Locate every blood parasite and identify its species.
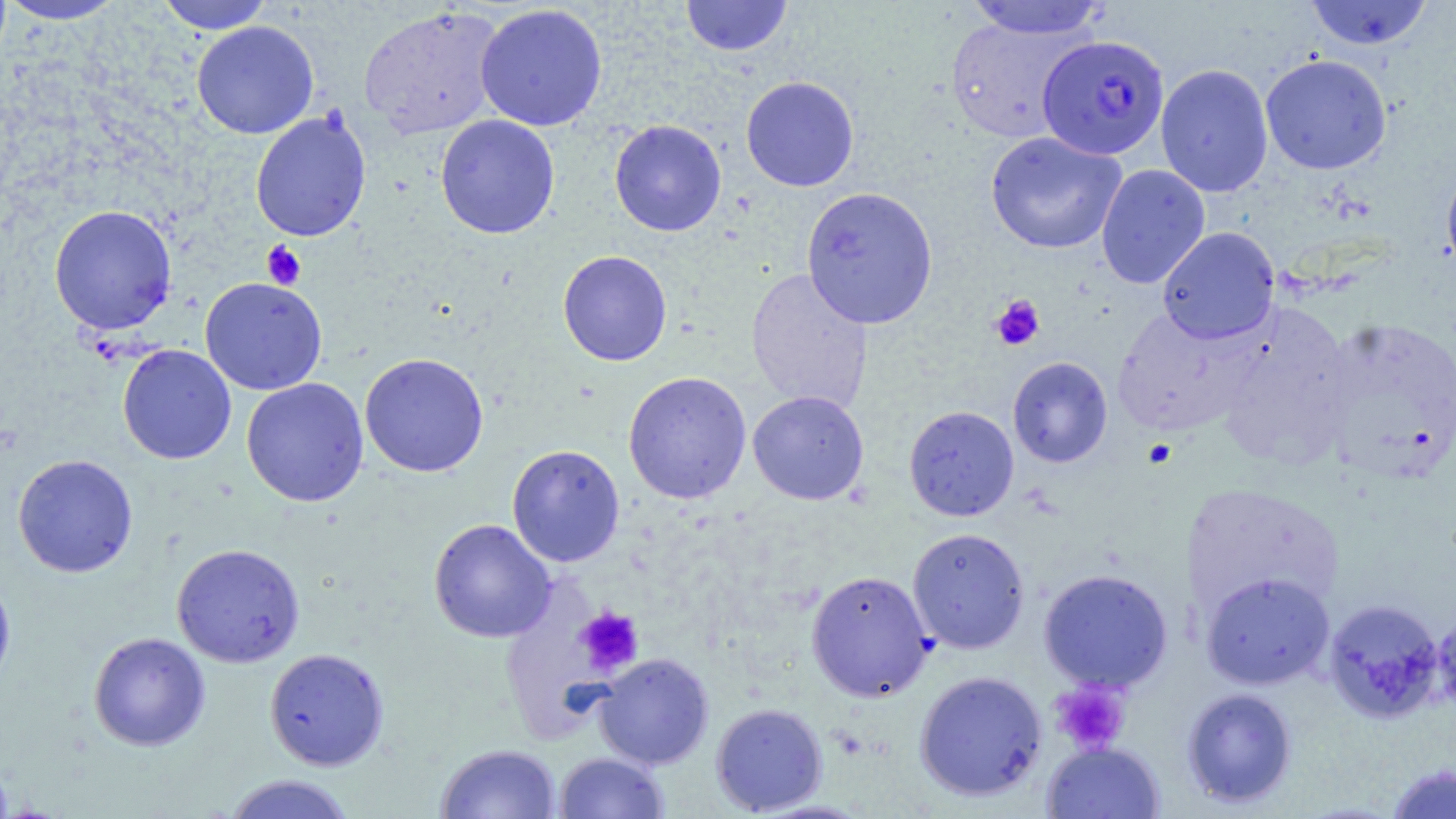

Approximate bounding boxes as [x1, y1, x2, y2] in pixels.
Plasmodium falciparum-infected red blood cells: [1037, 34, 1170, 160].
No Plasmodium ovale, Plasmodium malariae, Plasmodium vivax, Babesia divergens, or Trypanosoma brucei observed.

Platelet locations: [261, 241, 306, 289], [990, 294, 1046, 351], [1143, 438, 1177, 469], [575, 607, 644, 676], [1049, 680, 1130, 755]. Uninfected red blood cell locations: [157, 0, 276, 34], [680, 0, 794, 57], [963, 0, 1110, 40], [1304, 0, 1434, 50], [0, 1, 127, 25], [475, 4, 608, 131], [359, 6, 505, 138], [945, 15, 1089, 143], [191, 21, 319, 139], [1260, 54, 1392, 175], [1155, 64, 1274, 198], [740, 76, 859, 192], [250, 110, 371, 242], [435, 114, 560, 239], [609, 120, 726, 236], [984, 131, 1127, 254], [1441, 157, 1456, 285], [1095, 164, 1211, 289], [801, 186, 939, 329], [49, 205, 178, 335], [1157, 227, 1279, 344], [558, 250, 672, 366], [745, 267, 873, 415], [200, 277, 328, 396], [1212, 302, 1359, 469], [1111, 306, 1260, 436], [1317, 316, 1455, 483], [117, 344, 236, 465], [359, 352, 489, 477], [1007, 357, 1113, 468], [623, 371, 752, 504], [241, 377, 369, 506], [747, 390, 869, 505], [904, 405, 1019, 521], [507, 444, 625, 567], [12, 454, 138, 578], [1183, 481, 1344, 617], [428, 519, 556, 643], [907, 527, 1030, 654], [171, 543, 305, 668], [1039, 568, 1173, 692], [0, 569, 15, 694], [806, 570, 934, 701], [1200, 572, 1335, 689], [1323, 597, 1447, 724], [1431, 608, 1456, 717], [88, 632, 211, 751], [264, 648, 389, 770], [594, 653, 713, 769], [914, 670, 1047, 801], [1182, 687, 1298, 808], [710, 702, 828, 815], [1042, 741, 1165, 819], [435, 743, 560, 819], [554, 752, 669, 818], [1385, 763, 1455, 818], [222, 774, 358, 819]. Slide-level diagnosis: Plasmodium falciparum. 1000x magnification. Thin blood film. One field of a larger specimen. Light microscopy. May-Grünwald-Giemsa stain. Image is 1456×819 pixels.